Assess this cell for malaria.
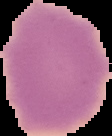

It is uninfected.

Image is 112×136 pixels. The area outside the segmented cell region is set to black. From a thin blood smear.